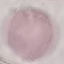
Summary:
  - Malaria status: uninfected
  - Image type: cell patch, automatically extracted from a larger field of view and resized to 64 × 64 pixels
  - Stain: Giemsa
  - Preparation: thin smear
  - Capture: smartphone through the microscope eyepiece